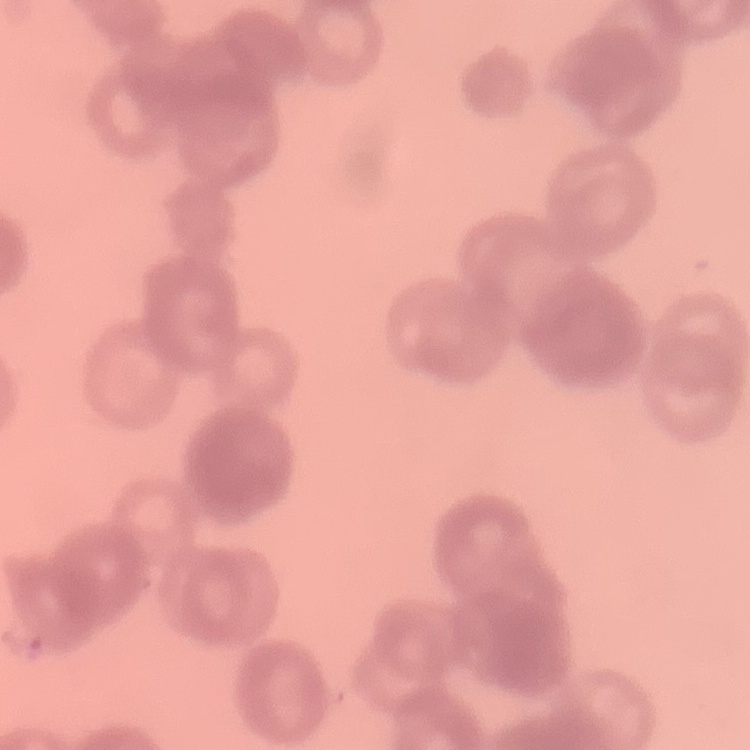

{
  "erythrocyte_morphology": "rouleaux formation",
  "image_type": "square crop of a larger photomicrograph",
  "preparation": "thin blood film",
  "stain": "Field's or Giemsa"
}